Point out each Plasmodium parasite.
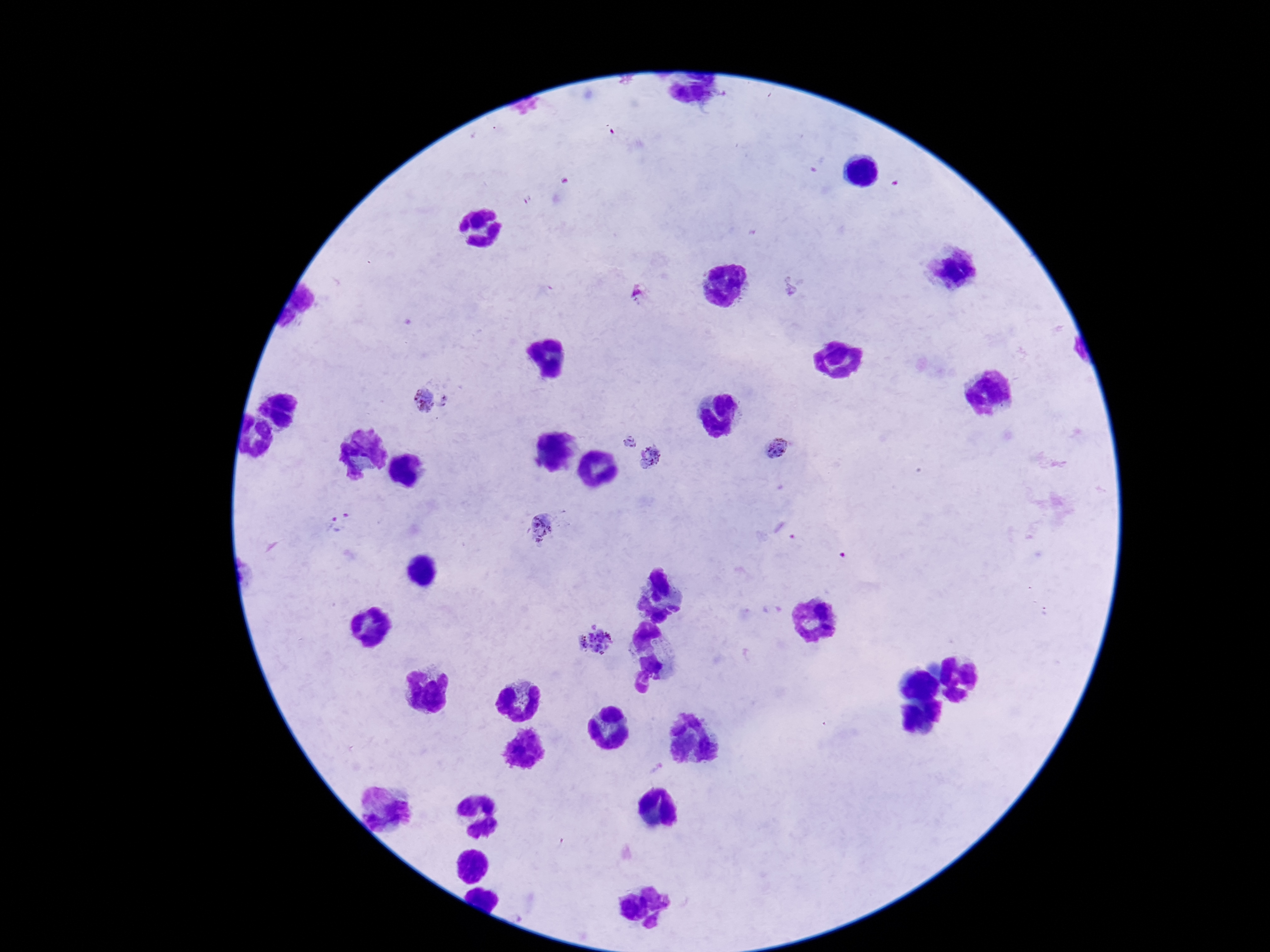
Approximate centers as (x, y) in pixels.
Plasmodium parasites: (641, 295), (431, 400), (628, 444), (775, 449), (651, 461), (340, 521), (542, 526), (598, 639).

stain = Giemsa
field of view = single
preparation = thick blood film
image size = 1270×952 pixels
patient malaria status = positive
capture = smartphone camera through the microscope eyepiece
magnification = 100x